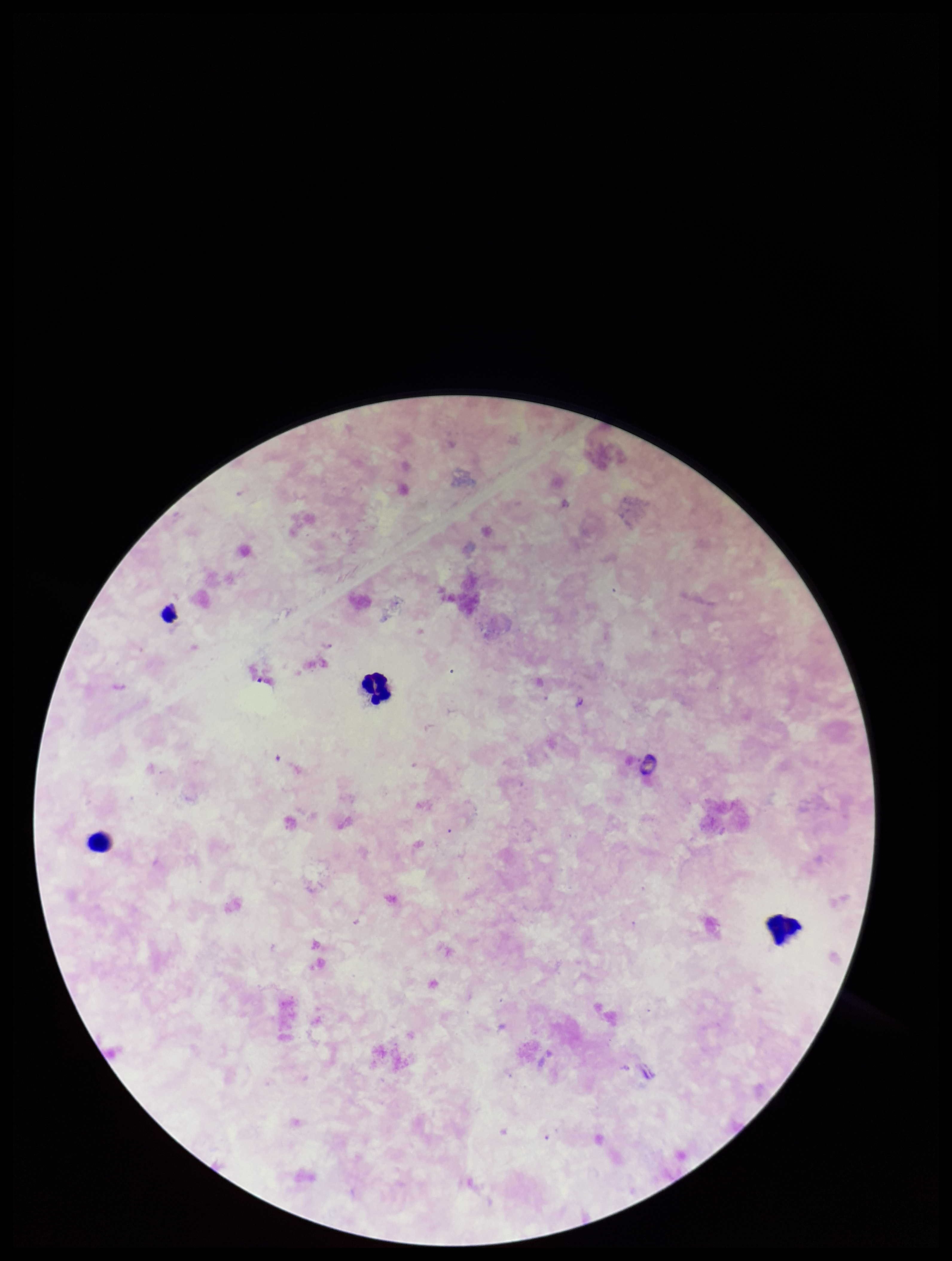
Leukocyte count: 3. Patient malaria status: negative. Smartphone photograph taken through the eyepiece of a microscope. Parasite count: 0. Preparation: thick blood smear. Plasmodium parasites: none seen. Image is 952×1261 pixels. Stained with Giemsa. One field from this slide.